Classify this cell by malaria status.
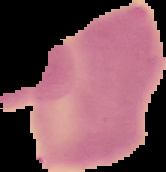

It is uninfected.

image_size: 166×172 pixels
image_type: cell region segmented out of the field of view; surrounding area masked to black
preparation: thin blood film